Identify the cell.
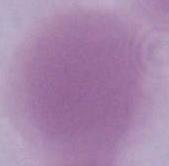

An erythrocyte.

Photomicrograph. Captured at 1000x magnification.